Give the position of every Plasmodium parasite.
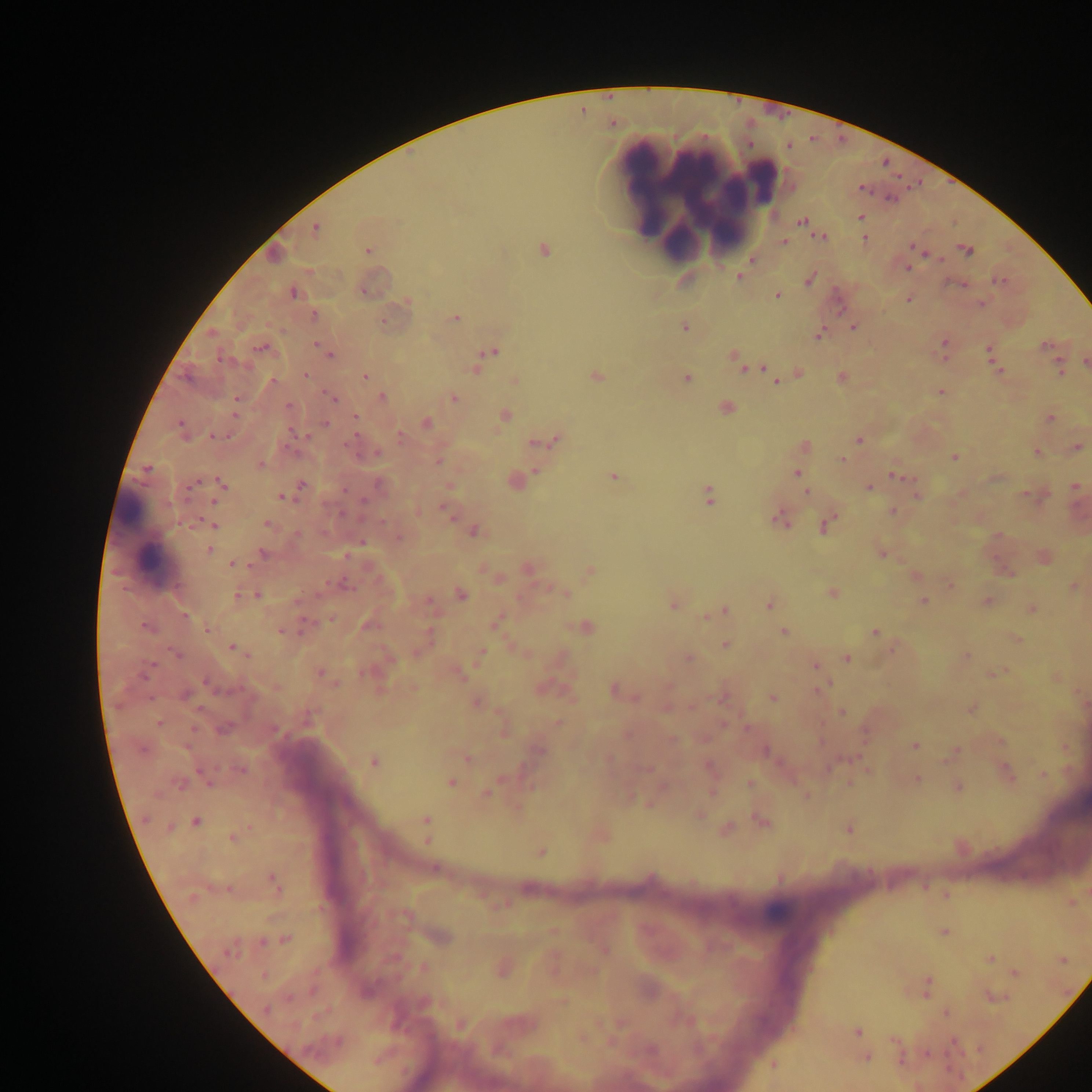
Approximate centers as {x, y} in pixels.
Plasmodium parasites: {860, 217}, {814, 228}, {864, 238}, {783, 241}, {910, 247}, {544, 250}, {963, 250}, {968, 252}, {925, 255}, {907, 268}, {739, 278}, {999, 280}, {994, 281}, {963, 284}, {293, 293}, {775, 295}, {908, 298}, {979, 303}, {311, 314}, {456, 319}, {383, 321}, {854, 326}, {945, 342}, {1045, 345}, {259, 347}, {987, 348}, {492, 350}, {222, 359}, {735, 359}, {1060, 364}, {474, 368}, {763, 371}, {1000, 371}, {1061, 372}, {596, 375}, {364, 376}, {685, 376}, {771, 377}, {273, 381}, {941, 392}, {382, 396}, {454, 398}, {236, 399}, {333, 399}, {288, 406}, {727, 407}, {357, 416}, {504, 417}, {1051, 418}, {324, 423}, {425, 423}, {180, 424}, {294, 431}, {304, 435}, {400, 436}, {554, 440}, {858, 440}, {531, 443}, {1075, 447}, {376, 452}, {1036, 453}, {953, 458}, {841, 459}, {147, 468}, {537, 471}, {890, 475}, {198, 481}, {221, 482}, {301, 486}, {1074, 486}, {868, 487}, {344, 489}, {708, 495}, {288, 496}, {281, 497}, {214, 501}, {363, 502}, {892, 511}, {779, 515}, {197, 521}, {190, 523}, {267, 524}, {212, 525}, {209, 549}, {262, 554}, {230, 564}, {257, 595}, {922, 600}, {428, 604}, {672, 605}, {1032, 615}, {185, 617}, {307, 624}, {145, 626}, {206, 630}, {281, 631}, {783, 631}, {875, 632}, {229, 646}, {481, 650}, {247, 657}, {847, 658}, {153, 664}, {814, 665}, {320, 674}, {999, 674}, {613, 691}, {771, 698}, {221, 729}, {193, 730}, {914, 745}, {956, 749}, {374, 759}, {243, 769}, {201, 771}, {1041, 775}, {918, 778}, {452, 782}, {748, 784}, {486, 794}, {711, 794}, {143, 819}, {427, 819}, {196, 823}, {170, 827}, {426, 839}, {434, 867}, {273, 879}, {946, 932}, {262, 941}, {229, 947}, {926, 978}, {925, 994}, {561, 1000}, {266, 1008}, {946, 1012}, {855, 1031}, {867, 1056}, {771, 1066}.

preparation = thick blood smear
leukocyte locations = approximate centers as {x, y} in pixels: {696, 189}, {143, 538}
capture = mobile-phone photograph through a microscope
field of view = single
image size = 1092×1092 pixels
country = Ghana